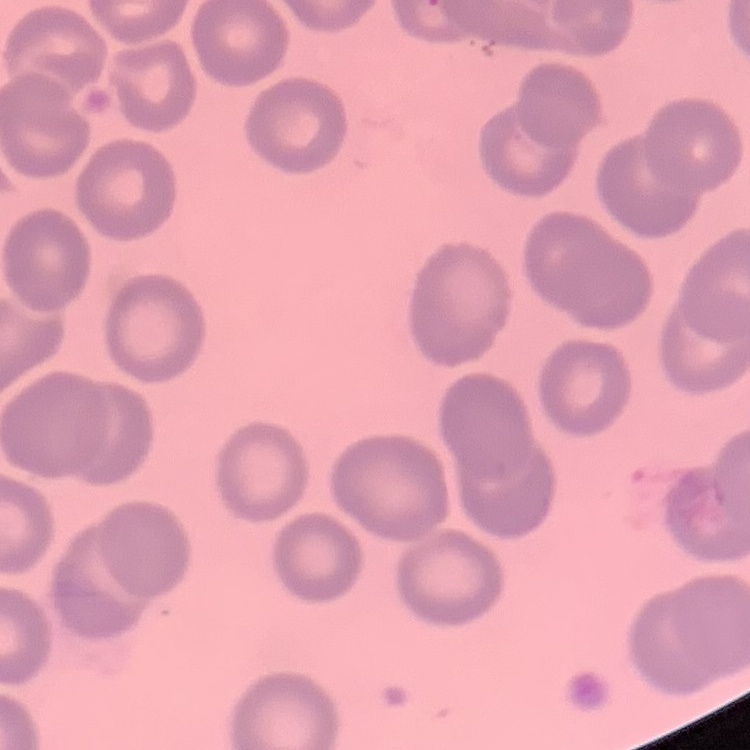 The red blood cells show no rouleaux formation. Thin blood smear. One tile cut from a larger photomicrograph. Stained with either Field's or Giemsa.